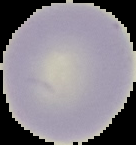
preparation = thin blood film
image type = segmented cell region with the area outside set to black
image size = 136×145 pixels
result = no Plasmodium parasites detected